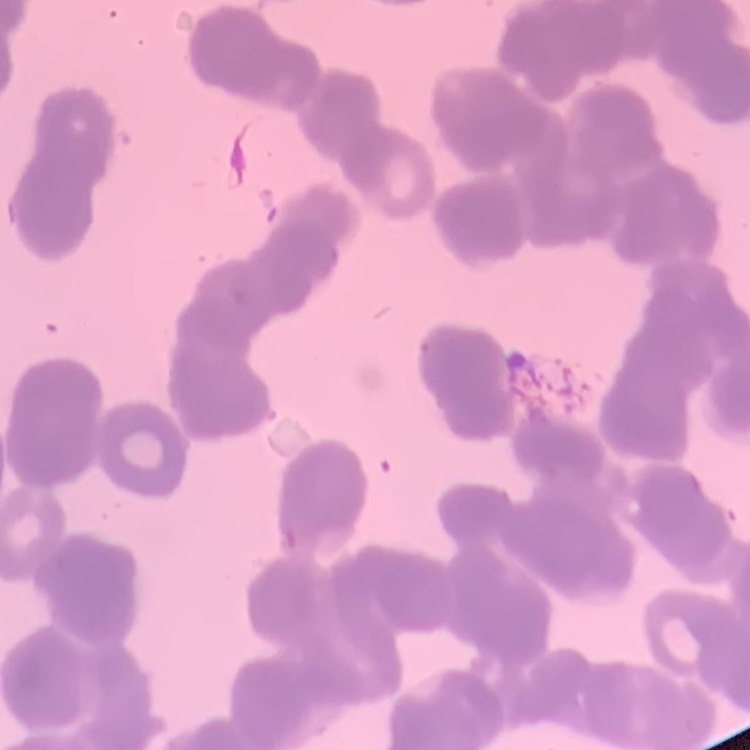

The red blood cells exhibit rouleaux formation. One tile cut from a larger photomicrograph. Thin blood film. Field's or Giemsa stain.